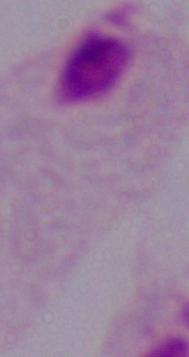
Summary:
  - Magnification: 1000x
  - Identification: trichomonad
  - Modality: micrograph